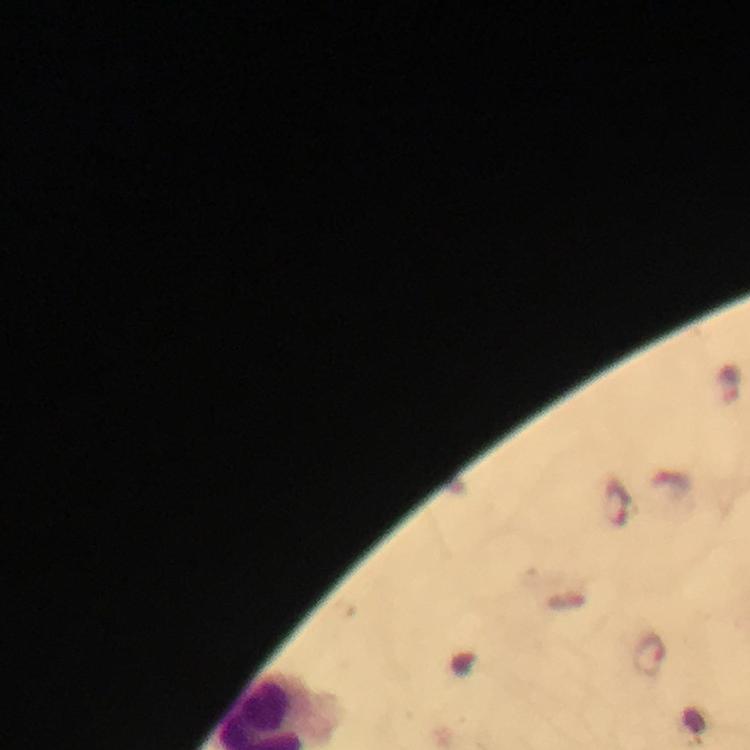

Approximate object centers, in pixels from the top-left corner. Plasmodium parasite locations: (x=730, y=384), (x=619, y=504), (x=650, y=654). Giemsa stain. Photographed through the microscope with a smartphone camera. Cropped region of a single field of view. Immersion oil was used. Thick smear. From a malaria diagnostic workup. Image is 750×750 pixels. At 100x magnification.